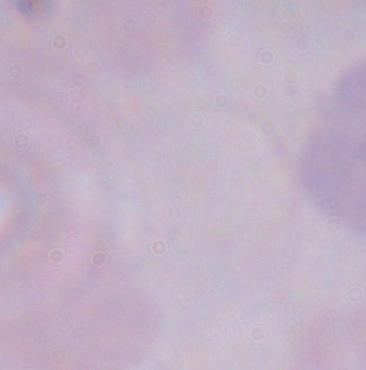
Summary:
  - Magnification: 1000x
  - Identification: trypanosome
  - Modality: photomicrograph